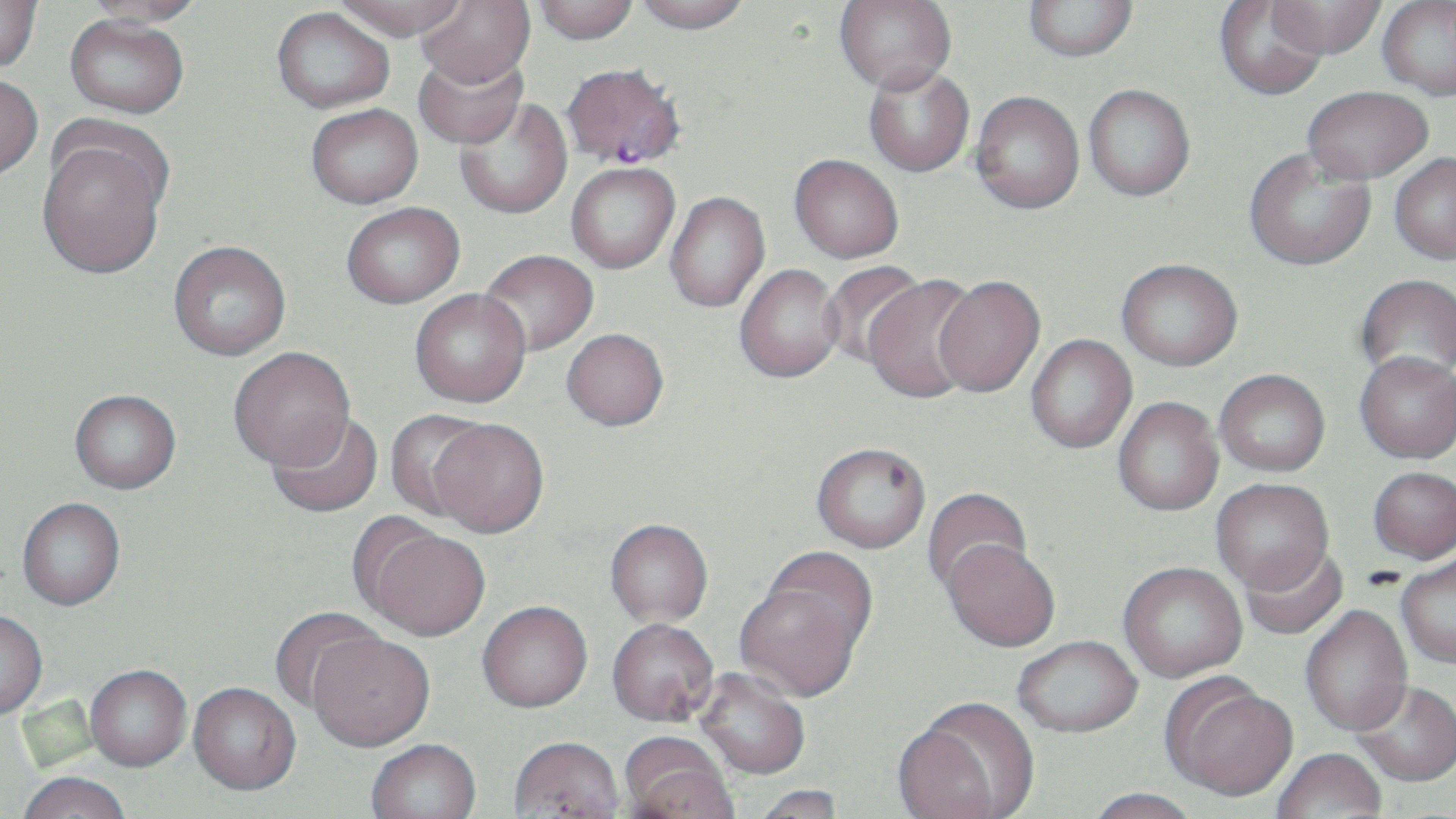

Approximate bounding boxes as (x1,y1)-(x2,y2) corner pairs in pixels. Plasmodium falciparum-infected red blood cell locations: (561,62)-(686,169). Uninfected red blood cell locations: (0,0)-(43,72), (334,0)-(466,40), (416,0)-(535,87), (531,0)-(639,44), (632,0)-(752,33), (834,0)-(956,93), (1023,0)-(1138,62), (1213,0)-(1329,101), (1267,0)-(1386,58), (82,1)-(208,28), (1378,1)-(1456,99), (271,7)-(395,113), (65,13)-(189,118), (414,49)-(528,150), (863,65)-(975,177), (0,74)-(43,180), (1083,84)-(1196,201), (1303,86)-(1433,183), (971,90)-(1085,214), (455,98)-(572,219), (306,103)-(423,208), (36,130)-(169,280), (1244,147)-(1375,270), (1390,153)-(1456,263), (789,154)-(904,263), (566,162)-(679,273), (665,191)-(770,313), (341,202)-(465,308), (168,240)-(291,360), (479,249)-(598,355), (1117,258)-(1242,370), (820,261)-(926,368), (734,264)-(843,382), (1355,274)-(1456,385), (862,275)-(982,403), (933,275)-(1045,398), (409,289)-(530,408), (561,328)-(669,430), (1026,335)-(1137,454), (229,346)-(356,469), (1354,351)-(1456,463), (1215,369)-(1330,476), (70,389)-(181,493), (1113,397)-(1224,516), (384,410)-(491,522), (267,412)-(384,519), (427,420)-(549,539), (811,443)-(929,552), (1368,466)-(1456,563), (1211,479)-(1333,595), (922,487)-(1033,597), (16,498)-(125,610), (604,521)-(713,629), (361,528)-(491,643), (941,540)-(1060,652), (1240,544)-(1349,640), (1396,554)-(1456,668), (1118,564)-(1247,682), (735,568)-(871,703), (478,604)-(593,716), (1301,605)-(1413,737), (269,607)-(383,712), (0,611)-(47,720), (607,621)-(719,729), (307,635)-(435,754), (1012,636)-(1143,739), (86,667)-(191,773), (694,669)-(810,781), (1163,680)-(1298,804), (1352,683)-(1456,789), (188,685)-(301,799), (894,703)-(1036,819), (508,740)-(624,818), (619,740)-(736,819), (367,741)-(482,819), (1272,751)-(1387,819), (18,775)-(131,819), (751,785)-(846,818), (1082,790)-(1204,819). Slide-level diagnosis: Plasmodium falciparum. Image is 1456×819 pixels. 1000x magnification. Optical microscopy. Single field of view. May-Grünwald-Giemsa-stained preparation. Thin blood smear.